Classify this cell by malaria status.
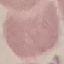

Uninfected.

Giemsa-stained preparation. Photographed with a smartphone camera at the microscope eyepiece. Cell patch, automatically extracted from a larger field of view and resized to 64 × 64 pixels. Thin blood film.